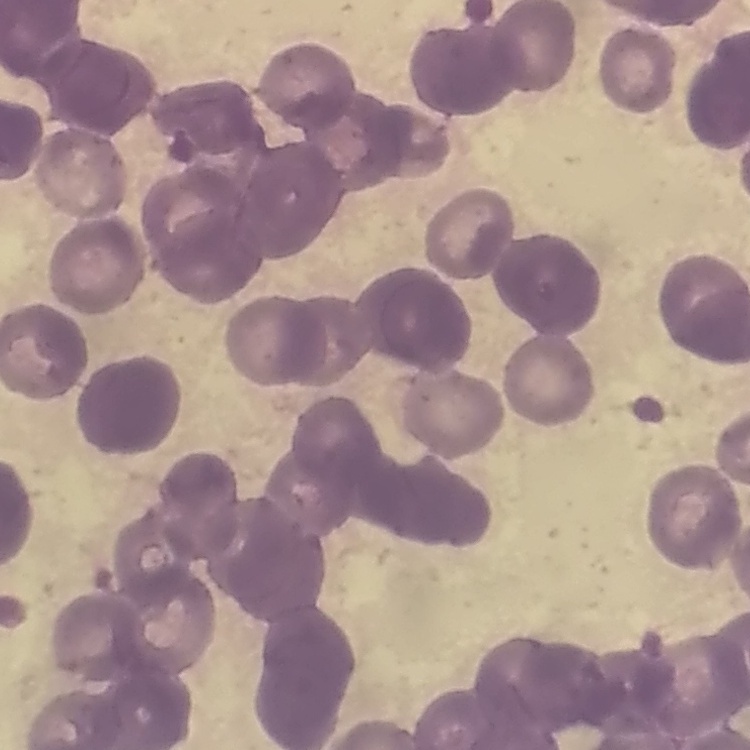
Summary:
  - Red blood cell morphology: rouleaux formation
  - Stain: Field's or Giemsa
  - Image type: square crop of a larger photomicrograph
  - Preparation: thin peripheral smear